State which parasite is depicted.
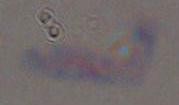

This is Toxoplasma gondii.

Summary:
  - Magnification: 1000x
  - Modality: photomicrograph